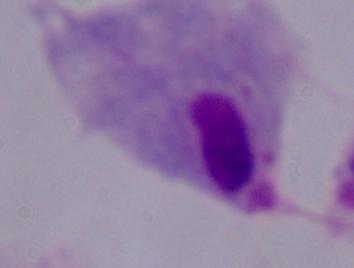

Summary:
  - Identification: trichomonad
  - Magnification: 1000x
  - Modality: photomicrograph